Assess the morphology of the erythrocytes.
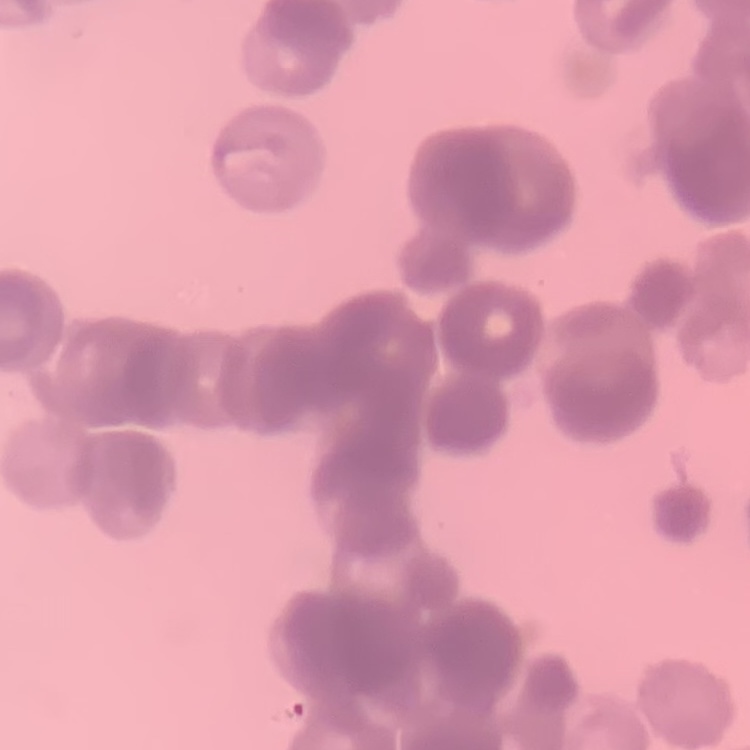
They show rouleaux formation.

Thin blood smear. Stained with either Field's or Giemsa. One tile cut from a larger photomicrograph.